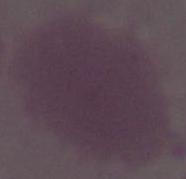

Micrograph. 1000x magnification. An erythrocyte is shown.